Outline each blood parasite and name the species.
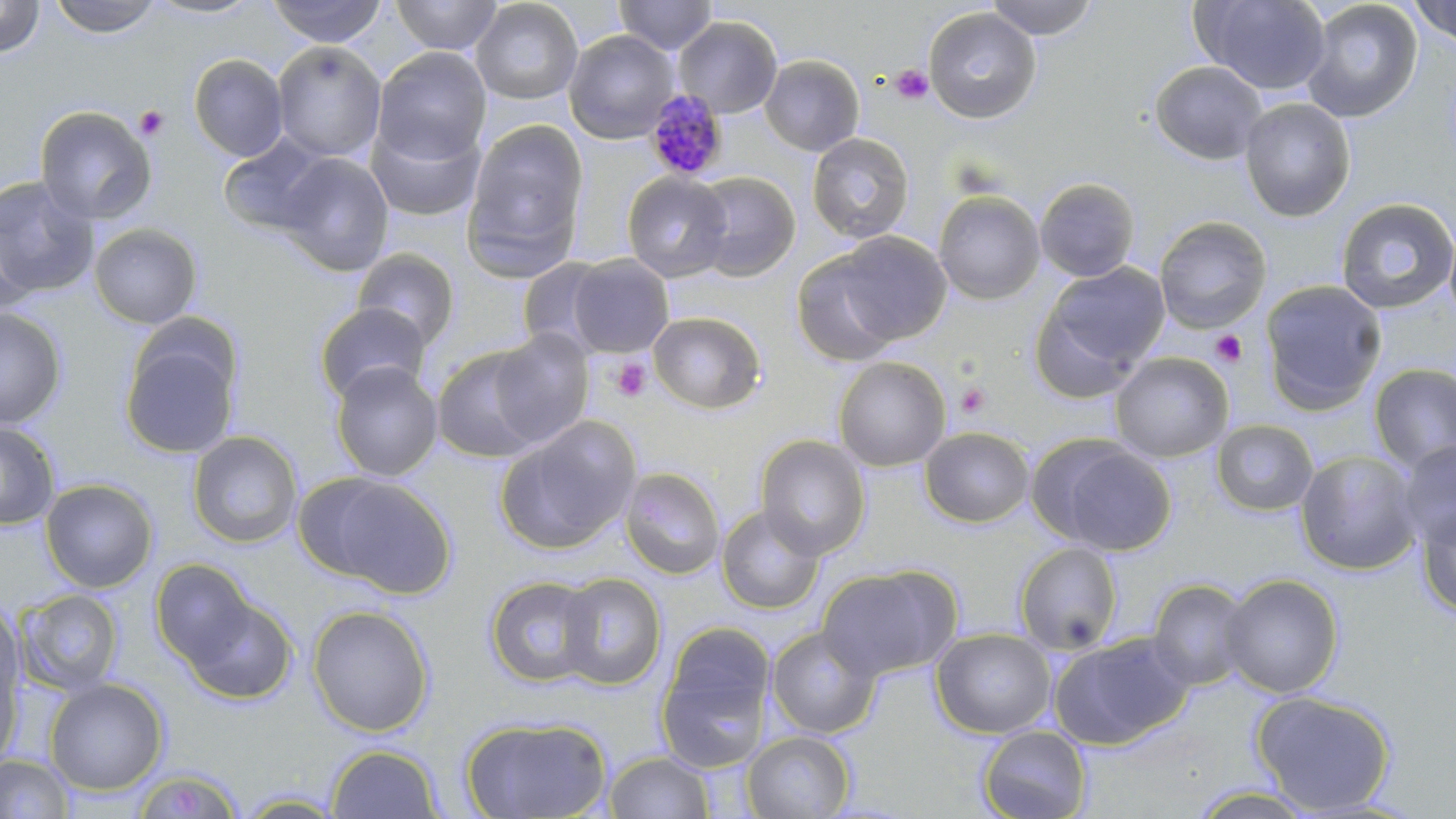

Approximate bounding boxes as (x1,y1)-(x2,y2) corner pairs in pixels.
Plasmodium malariae-infected red blood cells: (642,91)-(729,180).
No Plasmodium falciparum, Plasmodium ovale, Plasmodium vivax, Babesia divergens, or Trypanosoma brucei observed.

Summary:
  - Platelet locations: (890,64)-(933,105), (134,105)-(169,141), (1210,330)-(1248,368), (611,358)-(652,402), (954,381)-(991,419)
  - Uninfected red blood cell locations: (0,0)-(45,58), (48,0)-(162,37), (143,0)-(262,20), (268,0)-(386,47), (390,0)-(503,55), (470,0)-(583,104), (614,0)-(717,54), (984,0)-(1100,40), (1191,0)-(1331,95), (1302,1)-(1422,122), (1409,1)-(1456,46), (923,6)-(1042,123), (673,16)-(782,118), (564,29)-(679,143), (272,42)-(386,162), (373,46)-(491,164), (188,54)-(289,162), (759,54)-(865,156), (1149,60)-(1267,165), (1240,98)-(1356,222), (34,106)-(157,225), (366,118)-(486,222), (465,119)-(588,267), (807,132)-(914,244), (218,134)-(334,237), (276,152)-(394,277), (622,171)-(732,282), (691,171)-(801,281), (0,176)-(100,299), (1034,177)-(1141,282), (933,190)-(1045,304), (1335,198)-(1455,315), (0,215)-(37,316), (1154,216)-(1272,333), (88,223)-(203,329), (831,231)-(953,345), (352,249)-(460,350), (790,250)-(903,366), (568,254)-(673,357), (516,256)-(616,354), (1040,262)-(1170,381), (1259,279)-(1386,414), (314,302)-(431,403), (1029,302)-(1146,407), (0,308)-(66,429), (647,311)-(766,414), (487,329)-(596,448), (119,330)-(242,459), (432,346)-(549,463), (1110,352)-(1233,463), (832,356)-(951,471), (330,361)-(443,482), (1369,364)-(1456,470), (494,416)-(642,555), (1211,419)-(1319,517), (0,422)-(60,530), (919,426)-(1035,529), (187,430)-(303,549), (754,435)-(871,559), (1043,439)-(1176,555), (1396,439)-(1455,550), (1294,449)-(1423,575), (620,466)-(726,580), (303,473)-(456,596), (40,478)-(158,593), (1415,504)-(1456,619), (716,505)-(825,614), (1014,541)-(1124,655), (151,559)-(257,666), (817,565)-(959,681), (556,572)-(667,690), (1220,573)-(1343,699), (484,575)-(599,688), (1147,579)-(1254,690), (17,588)-(124,696), (179,592)-(298,706), (1,600)-(24,706), (307,604)-(435,736), (657,623)-(776,769), (765,625)-(881,739), (930,627)-(1056,738), (1050,634)-(1193,750), (0,657)-(23,773), (45,678)-(168,795), (1251,691)-(1396,814), (460,716)-(613,818), (977,725)-(1092,818), (741,730)-(856,818), (326,744)-(443,818), (603,750)-(716,818), (0,753)-(74,818), (131,768)-(246,818), (1185,786)-(1323,818), (231,790)-(348,817)
  - Slide-level diagnosis: Plasmodium malariae
  - Modality: optical microscopy
  - Image size: 1456×819 pixels
  - Magnification: 1000x
  - Stain: May-Grünwald-Giemsa
  - Preparation: thin blood film
  - Field of view: single